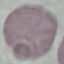
Result: no malaria parasites seen. Photographed with a smartphone camera at the microscope eyepiece. Thin blood film. Automatically extracted cell patch, resized to 64 × 64 pixels. Giemsa stain.